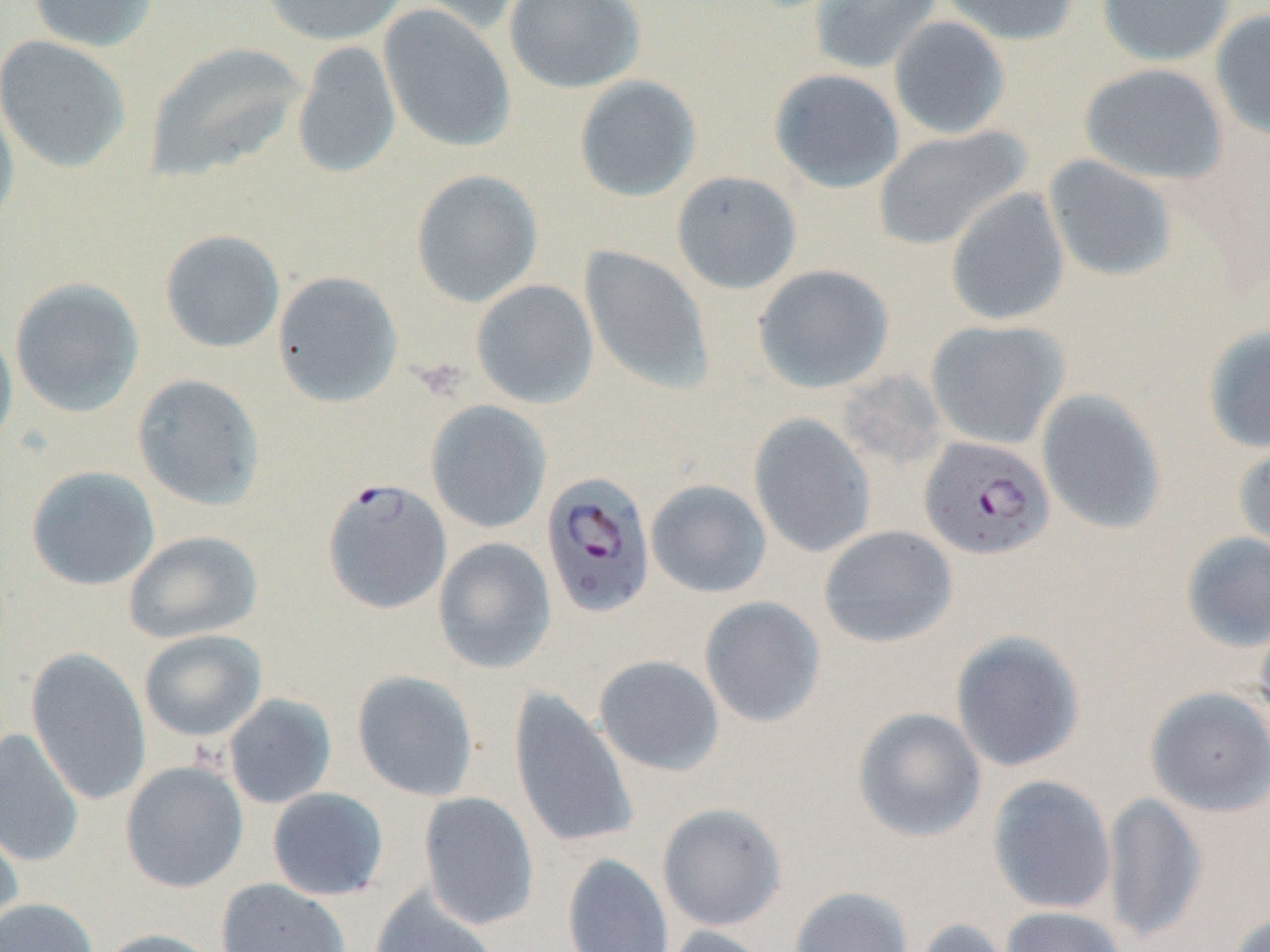 Approximate bounding boxes as [x1, y1, x2, y2] in pixels. Uninfected red blood cell locations: [27, 0, 159, 52], [259, 0, 408, 46], [409, 0, 532, 35], [503, 0, 646, 93], [809, 0, 943, 75], [940, 0, 1079, 45], [1096, 0, 1235, 66], [378, 5, 516, 153], [1210, 8, 1270, 140], [888, 16, 1011, 140], [1, 34, 132, 174], [292, 41, 401, 180], [144, 42, 307, 182], [1079, 63, 1228, 185], [769, 68, 904, 193], [574, 75, 701, 202], [0, 93, 21, 232], [871, 125, 1033, 252], [1043, 154, 1178, 282], [411, 169, 543, 307], [671, 170, 802, 294], [945, 187, 1070, 327], [160, 230, 285, 353], [579, 245, 714, 394], [752, 264, 894, 393], [272, 271, 403, 407], [9, 277, 144, 417], [471, 279, 599, 408], [924, 319, 1069, 450], [0, 322, 18, 457], [1203, 323, 1270, 454], [132, 374, 265, 510], [1036, 388, 1168, 535], [426, 400, 551, 534], [748, 413, 877, 558], [1233, 436, 1270, 561], [25, 465, 160, 590], [645, 479, 772, 599], [818, 525, 958, 648], [123, 530, 262, 644], [1180, 531, 1270, 651], [433, 537, 556, 675], [699, 596, 827, 728], [1253, 608, 1270, 738], [138, 629, 266, 742], [949, 630, 1086, 773], [25, 647, 152, 806], [593, 655, 725, 777], [352, 670, 479, 802], [1144, 685, 1270, 817], [507, 687, 640, 851], [223, 694, 337, 809], [852, 707, 987, 843], [0, 729, 84, 867], [120, 760, 248, 892], [986, 774, 1117, 915], [267, 787, 388, 901], [418, 791, 539, 930], [1103, 791, 1208, 944], [656, 802, 787, 931], [0, 813, 23, 942], [562, 853, 673, 952], [216, 878, 351, 952], [788, 886, 914, 952], [370, 887, 500, 952], [0, 898, 98, 952], [1000, 906, 1126, 952], [1225, 912, 1269, 952], [908, 917, 1020, 952], [659, 924, 776, 952], [93, 928, 222, 952]. Plasmodium falciparum-infected red blood cell locations: [919, 435, 1055, 560], [540, 470, 656, 618], [322, 477, 452, 614]. Slide-level diagnosis: Plasmodium falciparum. Thin blood film. Single field of view. Light microscopy. Image is 1270×952 pixels. May-Grünwald-Giemsa stain. Captured at 1000x magnification.